Give the extent of all Plasmodium vivax-infected red blood cells.
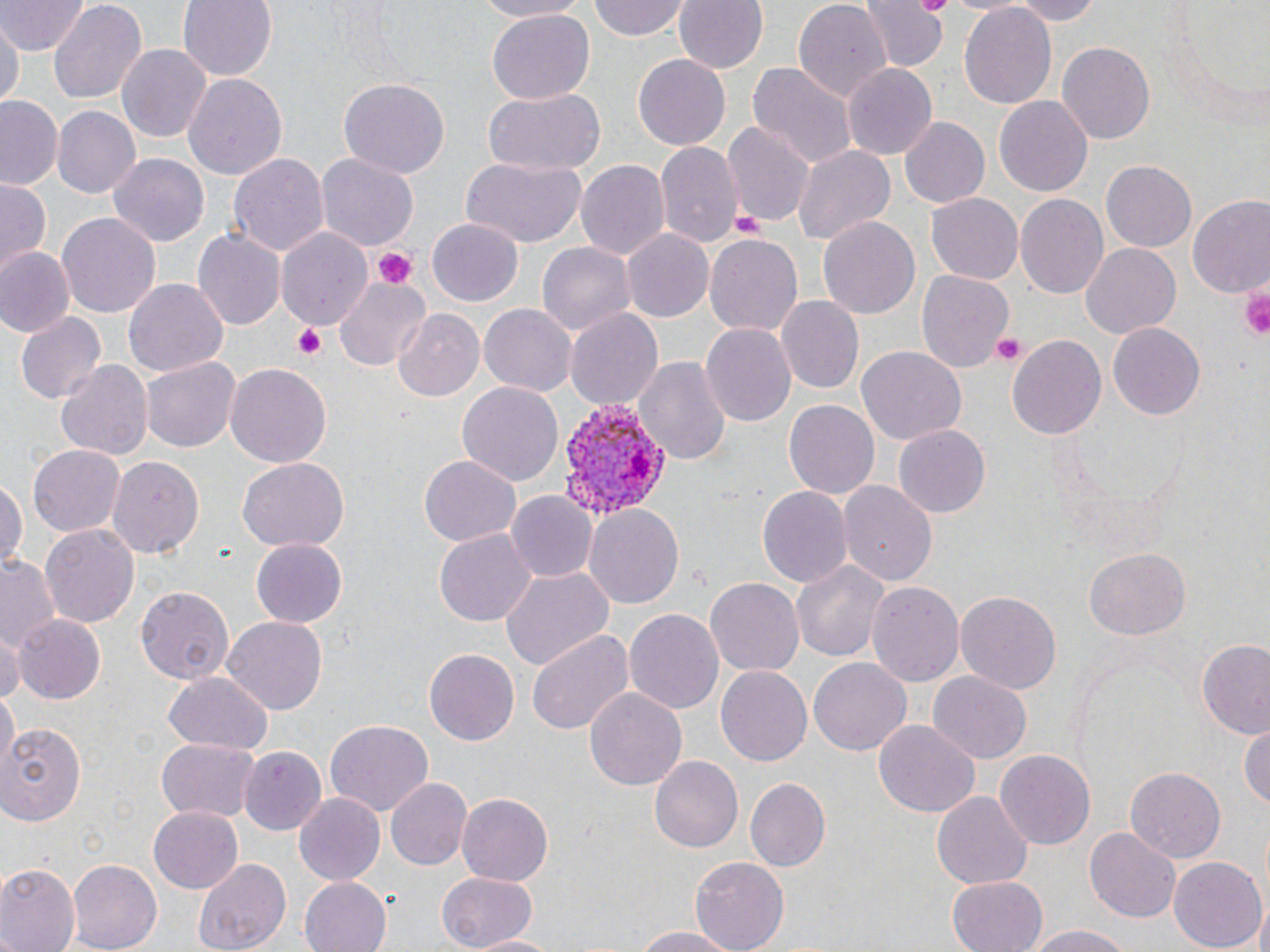
Approximate bounding boxes as named x1/y1/x2/y2 corners in pixels.
Plasmodium vivax-infected red blood cells: (x1=551, y1=395, x2=670, y2=520).

slide-level diagnosis = Plasmodium vivax
uninfected red blood cell locations = approximate bounding boxes as named x1/y1/x2/y2 corners in pixels: (x1=1, y1=0, x2=87, y2=54), (x1=49, y1=0, x2=148, y2=104), (x1=178, y1=0, x2=278, y2=81), (x1=472, y1=0, x2=592, y2=21), (x1=588, y1=0, x2=692, y2=42), (x1=674, y1=0, x2=768, y2=75), (x1=792, y1=0, x2=893, y2=103), (x1=860, y1=0, x2=946, y2=73), (x1=1002, y1=0, x2=1109, y2=24), (x1=1161, y1=0, x2=1270, y2=115), (x1=958, y1=2, x2=1057, y2=112), (x1=485, y1=10, x2=594, y2=105), (x1=1, y1=16, x2=20, y2=112), (x1=118, y1=42, x2=212, y2=144), (x1=1057, y1=42, x2=1154, y2=145), (x1=633, y1=52, x2=731, y2=149), (x1=749, y1=61, x2=855, y2=169), (x1=841, y1=63, x2=938, y2=158), (x1=184, y1=72, x2=287, y2=180), (x1=339, y1=79, x2=449, y2=179), (x1=484, y1=85, x2=606, y2=176), (x1=994, y1=96, x2=1092, y2=197), (x1=0, y1=97, x2=64, y2=192), (x1=54, y1=105, x2=142, y2=199), (x1=900, y1=116, x2=990, y2=207), (x1=724, y1=119, x2=815, y2=228), (x1=655, y1=140, x2=741, y2=246), (x1=793, y1=143, x2=896, y2=244), (x1=228, y1=148, x2=329, y2=258), (x1=108, y1=153, x2=212, y2=247), (x1=315, y1=154, x2=418, y2=252), (x1=459, y1=157, x2=587, y2=247), (x1=576, y1=159, x2=671, y2=262), (x1=1101, y1=161, x2=1197, y2=252), (x1=1, y1=177, x2=53, y2=271), (x1=926, y1=190, x2=1022, y2=282), (x1=1016, y1=193, x2=1108, y2=301), (x1=1187, y1=198, x2=1270, y2=303), (x1=57, y1=212, x2=161, y2=318), (x1=817, y1=216, x2=919, y2=321), (x1=424, y1=217, x2=525, y2=308), (x1=278, y1=227, x2=372, y2=334), (x1=623, y1=228, x2=713, y2=322), (x1=195, y1=229, x2=286, y2=331), (x1=704, y1=231, x2=803, y2=334), (x1=538, y1=241, x2=636, y2=336), (x1=1081, y1=243, x2=1181, y2=337), (x1=1, y1=248, x2=72, y2=335), (x1=918, y1=270, x2=1014, y2=371), (x1=333, y1=274, x2=431, y2=373), (x1=124, y1=279, x2=227, y2=377), (x1=775, y1=296, x2=863, y2=396), (x1=480, y1=303, x2=578, y2=397), (x1=392, y1=309, x2=483, y2=402), (x1=564, y1=309, x2=661, y2=413), (x1=14, y1=312, x2=105, y2=406), (x1=702, y1=322, x2=796, y2=429), (x1=1108, y1=322, x2=1205, y2=419), (x1=1008, y1=336, x2=1107, y2=441), (x1=857, y1=344, x2=965, y2=443), (x1=635, y1=355, x2=730, y2=466), (x1=141, y1=356, x2=240, y2=453), (x1=55, y1=359, x2=151, y2=463), (x1=226, y1=363, x2=331, y2=468), (x1=457, y1=380, x2=563, y2=487), (x1=783, y1=399, x2=880, y2=500), (x1=896, y1=424, x2=991, y2=516), (x1=27, y1=445, x2=123, y2=537), (x1=105, y1=452, x2=203, y2=557), (x1=419, y1=456, x2=522, y2=547), (x1=236, y1=458, x2=349, y2=553), (x1=0, y1=476, x2=26, y2=572), (x1=838, y1=481, x2=938, y2=586), (x1=756, y1=486, x2=850, y2=588), (x1=506, y1=491, x2=597, y2=583), (x1=584, y1=504, x2=685, y2=609), (x1=39, y1=523, x2=139, y2=628), (x1=435, y1=529, x2=534, y2=627), (x1=250, y1=538, x2=345, y2=628), (x1=1082, y1=548, x2=1190, y2=639), (x1=0, y1=557, x2=63, y2=650), (x1=791, y1=558, x2=892, y2=664), (x1=501, y1=566, x2=613, y2=672), (x1=706, y1=578, x2=803, y2=677), (x1=867, y1=580, x2=964, y2=690), (x1=136, y1=586, x2=234, y2=685), (x1=956, y1=590, x2=1061, y2=696), (x1=625, y1=609, x2=723, y2=717), (x1=13, y1=615, x2=105, y2=702), (x1=221, y1=617, x2=328, y2=713), (x1=1, y1=629, x2=21, y2=706), (x1=527, y1=630, x2=635, y2=736), (x1=1198, y1=643, x2=1270, y2=739), (x1=423, y1=649, x2=517, y2=746), (x1=810, y1=656, x2=910, y2=756), (x1=717, y1=665, x2=811, y2=767), (x1=927, y1=670, x2=1031, y2=763), (x1=164, y1=672, x2=273, y2=753), (x1=583, y1=687, x2=687, y2=792), (x1=1, y1=688, x2=17, y2=774), (x1=2, y1=719, x2=87, y2=826), (x1=326, y1=719, x2=433, y2=814), (x1=874, y1=720, x2=979, y2=817), (x1=1241, y1=722, x2=1270, y2=812), (x1=156, y1=739, x2=260, y2=821), (x1=238, y1=745, x2=327, y2=836), (x1=994, y1=748, x2=1096, y2=849), (x1=650, y1=756, x2=743, y2=854), (x1=1124, y1=767, x2=1225, y2=864), (x1=386, y1=776, x2=471, y2=870), (x1=744, y1=777, x2=829, y2=872), (x1=930, y1=791, x2=1032, y2=890), (x1=294, y1=792, x2=386, y2=885), (x1=456, y1=794, x2=554, y2=883), (x1=148, y1=806, x2=243, y2=893), (x1=1086, y1=827, x2=1181, y2=921), (x1=1167, y1=855, x2=1267, y2=952), (x1=194, y1=857, x2=292, y2=952), (x1=689, y1=857, x2=788, y2=952), (x1=68, y1=860, x2=162, y2=950), (x1=0, y1=866, x2=78, y2=952), (x1=436, y1=871, x2=540, y2=950), (x1=946, y1=875, x2=1047, y2=952), (x1=297, y1=876, x2=393, y2=952), (x1=1247, y1=899, x2=1270, y2=952), (x1=1024, y1=924, x2=1137, y2=952), (x1=629, y1=926, x2=742, y2=951), (x1=464, y1=934, x2=569, y2=951)
modality = light microscopy
stain = May-Grünwald-Giemsa
platelet locations = approximate bounding boxes as named x1/y1/x2/y2 corners in pixels: (x1=730, y1=211, x2=765, y2=239), (x1=373, y1=246, x2=418, y2=286), (x1=1241, y1=278, x2=1270, y2=342), (x1=292, y1=322, x2=328, y2=360), (x1=989, y1=333, x2=1028, y2=367)
magnification = 1000x
preparation = thin blood smear
image size = 1270×952 pixels
field of view = single